Comment on the morphology of the red blood cells.
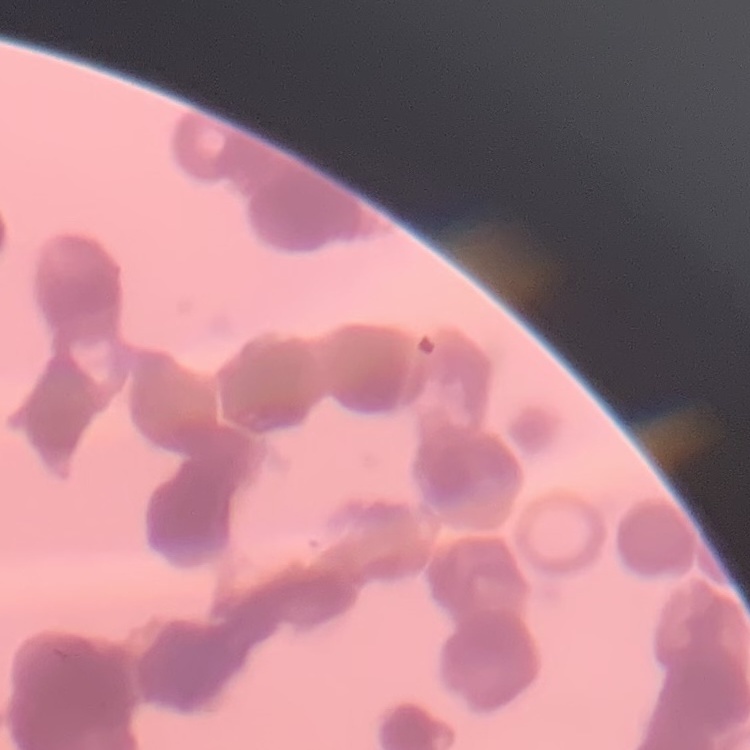

They show rouleaux formation.

Summary:
  - Image type: one tile cut from a larger photomicrograph
  - Preparation: thin blood smear
  - Stain: Field's or Giemsa